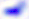
magnification = 400x
identification = Toxoplasma gondii
modality = micrograph